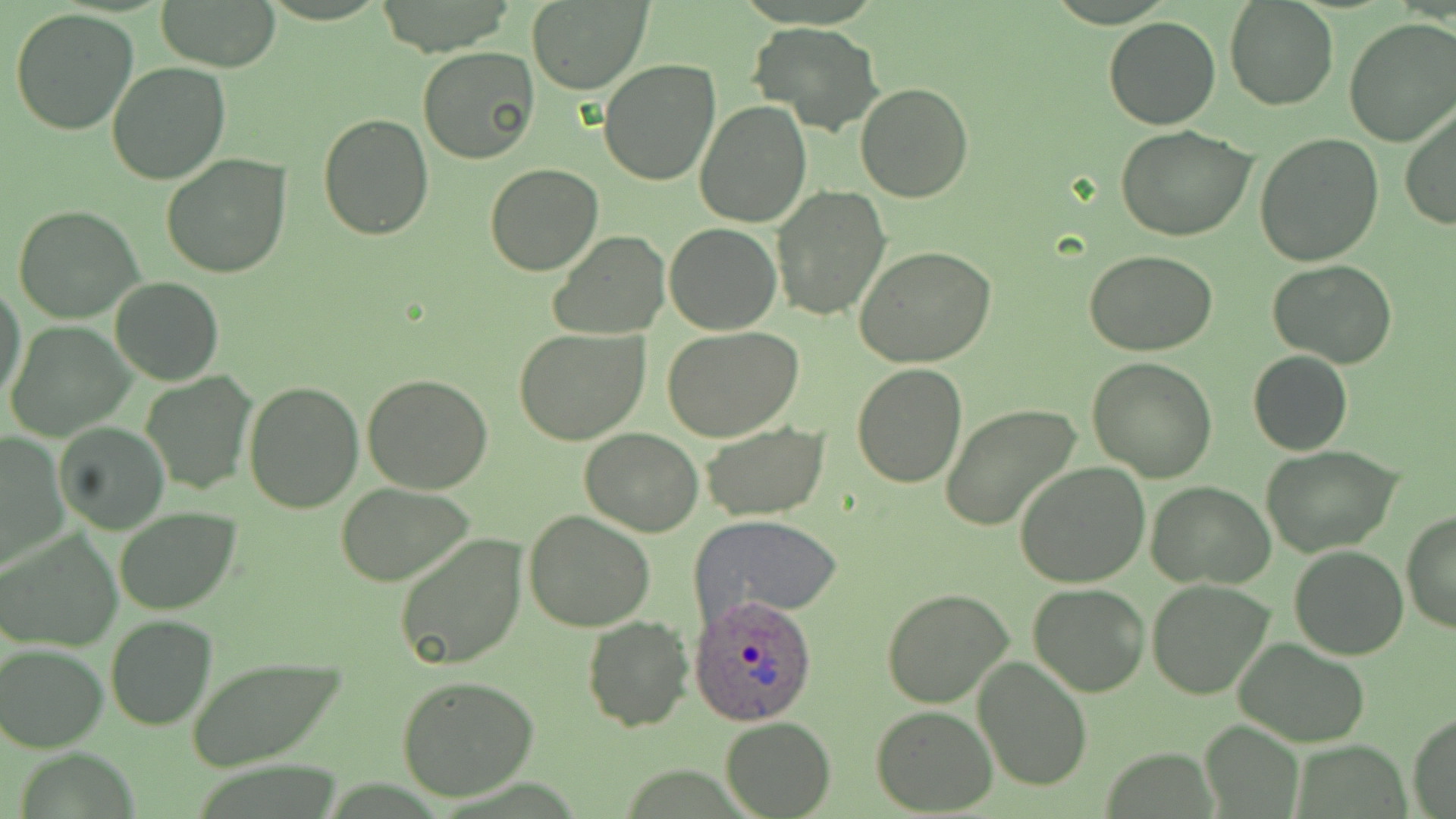
slide_level_diagnosis: Plasmodium ovale
field_of_view: single
image_size: 1456×819 pixels
plasmodium_ovale_infected_red_blood_cell_locations: 'approximate bounding boxes as (x1,y1)-(x2,y2) corner pairs in pixels: (688,594)-(820,726)'
modality: light microscopy
magnification: 1000x
uninfected_red_blood_cell_locations: 'approximate bounding boxes as (x1,y1)-(x2,y2) corner pairs in pixels: (155,0)-(282,72), (1224,0)-(1339,112), (527,1)-(650,93), (10,8)-(140,136), (1102,17)-(1220,130), (1343,18)-(1456,146), (748,21)-(883,135), (417,46)-(540,165), (598,58)-(721,186), (106,62)-(232,185), (855,82)-(974,202), (695,102)-(811,228), (1400,105)-(1456,231), (317,114)-(435,241), (1114,125)-(1258,242), (1253,134)-(1384,266), (161,155)-(291,278), (484,164)-(602,277), (770,185)-(891,322), (13,204)-(144,324), (664,221)-(781,334), (550,232)-(672,341), (854,245)-(997,369), (1084,251)-(1216,356), (1268,259)-(1397,369), (110,276)-(225,386), (0,283)-(28,404), (6,322)-(133,441), (513,328)-(651,447), (663,328)-(805,442), (1248,350)-(1353,457), (1087,356)-(1218,481), (850,363)-(968,488), (140,371)-(256,494), (362,373)-(494,494), (242,381)-(364,514), (940,404)-(1083,534), (52,420)-(171,535), (700,423)-(828,521), (578,428)-(704,537), (1,430)-(70,570), (1262,445)-(1403,557), (1014,462)-(1152,589), (334,482)-(475,586), (1147,482)-(1276,587), (115,508)-(241,615), (525,509)-(655,630), (1400,509)-(1456,634), (689,513)-(845,628), (2,531)-(122,653), (395,533)-(529,671), (1288,546)-(1410,661), (1146,578)-(1275,699), (1027,582)-(1149,698), (881,588)-(1014,708), (105,615)-(217,731), (582,616)-(694,732), (1233,637)-(1371,746), (1,642)-(108,750), (186,656)-(340,769), (972,656)-(1091,791), (394,676)-(540,803), (870,706)-(997,814), (1409,714)-(1453,817), (720,716)-(835,818), (1200,719)-(1302,817)'
stain: May-Grünwald-Giemsa
preparation: thin blood smear